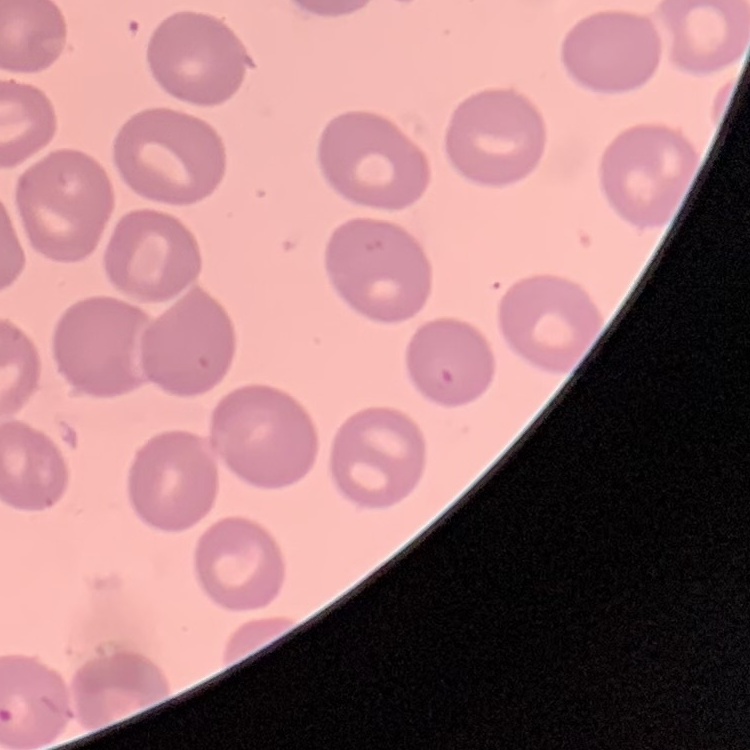
{
  "red_blood_cell_morphology": "no rouleaux formation",
  "stain": "Field's or Giemsa",
  "preparation": "thin peripheral smear",
  "image_type": "one tile cut from a larger photomicrograph"
}